Draw a bounding box around every Plasmodium parasite.
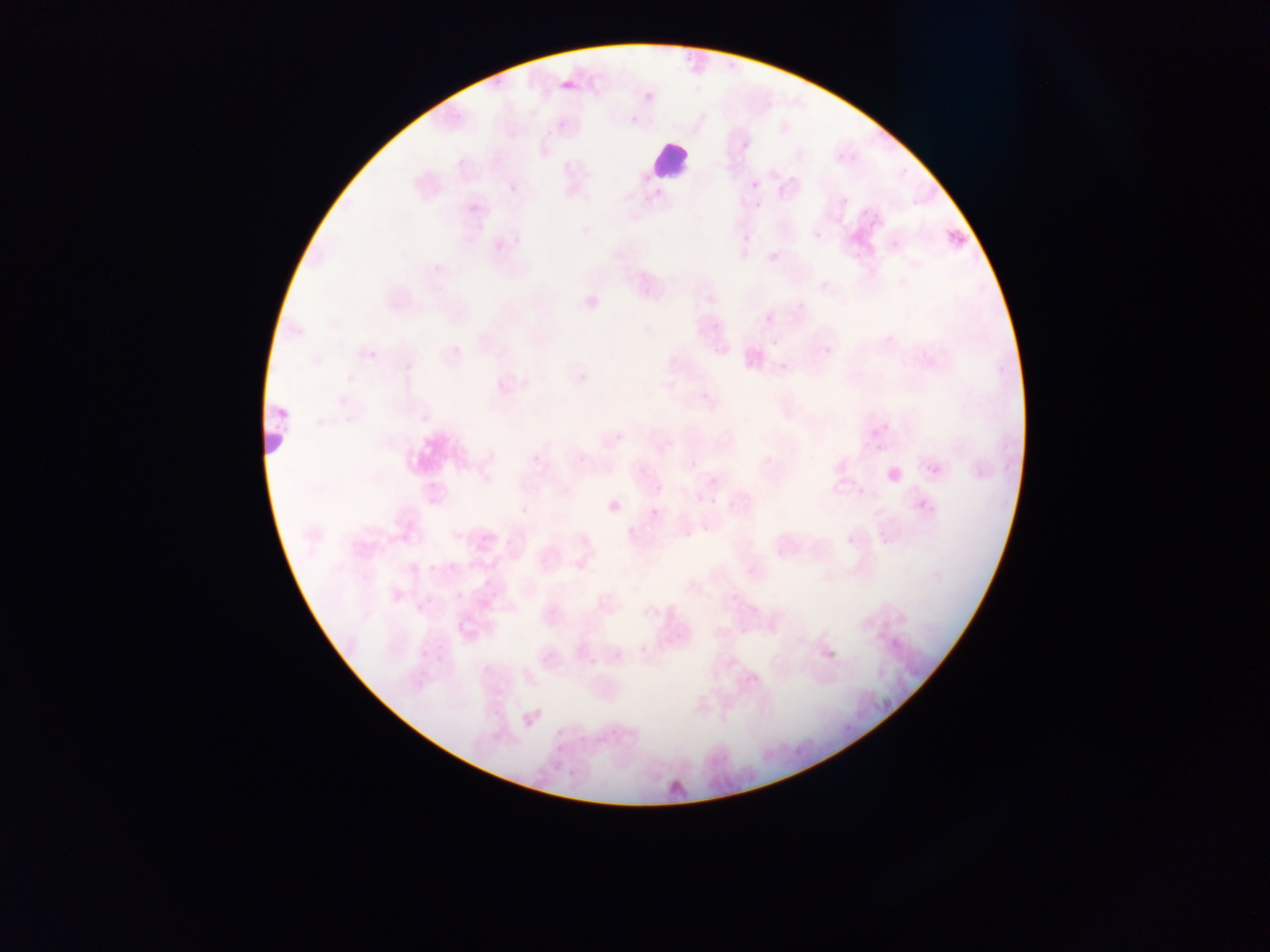
Approximate bounding boxes as left top right bottom in pixels.
Plasmodium parasites: 559 73 573 94; 641 91 654 102; 750 180 761 191; 944 225 971 253; 815 230 823 239; 764 314 774 324; 767 336 779 350; 818 348 832 357; 868 423 884 437; 922 461 940 474; 915 500 926 508; 649 507 662 520; 825 640 845 661; 584 660 595 671; 841 722 852 735; 554 735 570 754.

Leukocyte locations: 650 139 693 182; 260 399 289 460. Collected in Ghana. One field of view. Image is 1270×952 pixels. Thin blood film. Mobile-phone photograph taken through the microscope.